Locate every malaria parasite.
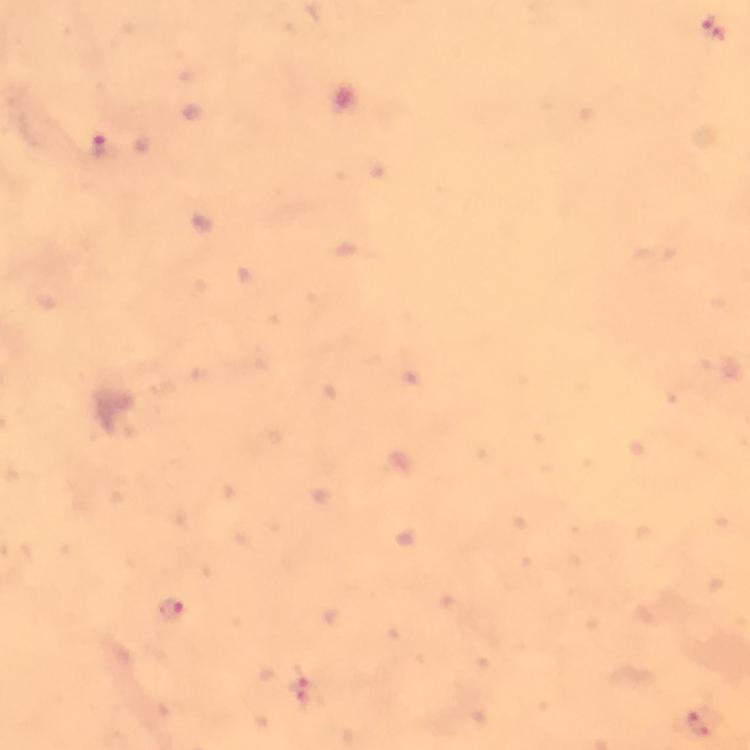
Approximate object centers, in pixels from the top-left corner.
Malaria parasites: (x=711, y=29), (x=98, y=144), (x=170, y=609), (x=302, y=688).

Summary:
  - Stain: Giemsa
  - Image size: 750×750 pixels
  - Cropped from: one field of view
  - Magnification: 100x
  - Preparation: thick smear
  - Context: from a malaria diagnostic workup
  - Immersion oil: applied
  - Capture: smartphone camera through the microscope